Assess this cell for malaria.
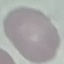

It is uninfected.

Photographed with a smartphone camera at the microscope eyepiece. Giemsa-stained preparation. Thin blood film. Automatically extracted cell patch, resized to 64 × 64 pixels.